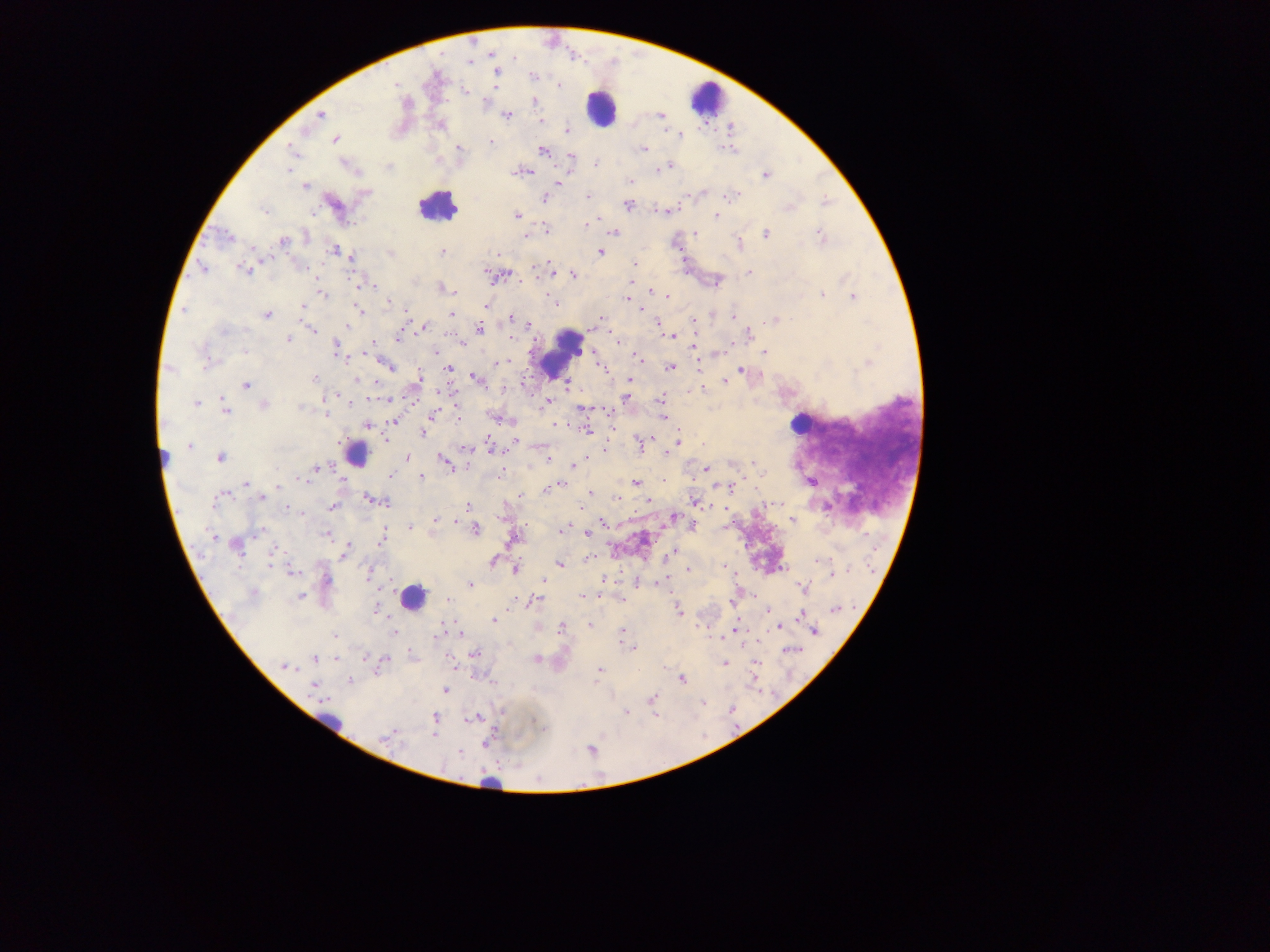

leukocyte locations = approximate centers as {x, y} in pixels: {706, 97}, {602, 108}, {437, 207}, {560, 351}, {799, 423}, {357, 457}, {413, 597}, {325, 723}, {491, 785}
preparation = thick blood smear
field of view = single
Plasmodium parasite locations = approximate centers as {x, y} in pixels: {514, 59}, {470, 62}, {495, 72}, {532, 76}, {395, 84}, {559, 85}, {465, 92}, {533, 103}, {320, 115}, {507, 115}, {661, 116}, {541, 122}, {568, 130}, {680, 135}, {335, 139}, {490, 142}, {459, 148}, {291, 149}, {644, 149}, {542, 150}, {571, 157}, {596, 163}, {669, 166}, {288, 170}, {658, 170}, {519, 172}, {765, 176}, {630, 181}, {558, 183}, {304, 186}, {366, 192}, {588, 196}, {545, 197}, {731, 197}, {824, 201}, {628, 206}, {789, 206}, {263, 210}, {517, 215}, {716, 216}, {585, 225}, {546, 230}, {614, 233}, {696, 233}, {765, 234}, {820, 234}, {306, 235}, {527, 235}, {228, 236}, {283, 241}, {739, 244}, {334, 251}, {442, 252}, {599, 253}, {390, 254}, {499, 254}, {351, 257}, {635, 264}, {202, 268}, {535, 268}, {244, 270}, {486, 272}, {748, 272}, {574, 275}, {359, 284}, {370, 286}, {442, 288}, {652, 292}, {454, 293}, {322, 294}, {822, 294}, {853, 296}, {668, 297}, {625, 299}, {552, 300}, {389, 302}, {555, 303}, {486, 306}, {303, 307}, {639, 308}, {184, 309}, {359, 311}, {406, 312}, {451, 314}, {267, 316}, {733, 317}, {511, 318}, {599, 319}, {775, 319}, {657, 321}, {693, 321}, {348, 325}, {529, 325}, {423, 328}, {313, 329}, {480, 329}, {224, 332}, {749, 333}, {670, 336}, {398, 338}, {511, 338}, {288, 340}, {618, 341}, {461, 343}, {335, 346}, {370, 346}, {695, 346}, {245, 351}, {435, 351}, {765, 353}, {363, 355}, {636, 357}, {206, 360}, {504, 362}, {499, 363}, {867, 364}, {390, 366}, {672, 367}, {170, 369}, {448, 369}, {741, 370}, {474, 377}, {315, 379}, {356, 380}, {417, 380}, {630, 380}, {726, 381}, {376, 383}, {246, 385}, {566, 385}, {701, 388}, {625, 398}, {661, 399}, {350, 401}, {549, 402}, {196, 403}, {264, 404}, {225, 409}, {581, 409}, {325, 414}, {432, 415}, {662, 417}, {458, 418}, {394, 420}, {556, 425}, {367, 426}, {587, 430}, {424, 432}, {678, 440}, {516, 441}, {639, 444}, {189, 446}, {492, 448}, {669, 453}, {220, 458}, {406, 458}, {549, 458}, {442, 459}, {753, 462}, {576, 464}, {315, 468}, {573, 468}, {706, 470}, {500, 474}, {390, 476}, {422, 477}, {299, 479}, {635, 483}, {247, 484}, {558, 485}, {278, 486}, {547, 489}, {589, 492}, {223, 495}, {520, 496}, {261, 497}, {617, 498}, {370, 499}, {385, 502}, {649, 502}, {695, 502}, {214, 503}, {468, 506}, {332, 507}, {289, 509}, {301, 514}, {674, 517}, {792, 520}, {436, 521}, {454, 521}, {602, 522}, {410, 527}, {475, 529}, {563, 530}, {259, 531}, {587, 534}, {327, 535}, {213, 537}, {380, 539}, {237, 547}, {273, 550}, {344, 554}, {672, 554}, {816, 561}, {494, 562}, {559, 564}, {270, 565}, {723, 566}, {515, 570}, {689, 570}, {292, 571}, {831, 576}, {326, 579}, {544, 580}, {470, 585}, {803, 588}, {583, 596}, {300, 597}, {448, 600}, {535, 601}, {376, 609}, {835, 610}, {678, 611}, {799, 616}, {494, 620}, {589, 625}, {779, 627}, {561, 628}, {622, 631}, {814, 631}, {393, 632}, {437, 635}, {335, 636}, {632, 648}, {475, 654}, {315, 659}, {335, 659}, {537, 659}, {725, 664}, {285, 666}, {599, 670}, {682, 679}, {350, 680}, {314, 687}, {445, 691}, {326, 698}, {653, 699}, {626, 712}, {434, 717}, {475, 718}, {433, 736}, {387, 737}, {486, 743}, {459, 752}
capture = mobile-phone photograph through a microscope
image size = 1270×952 pixels
country = Ghana